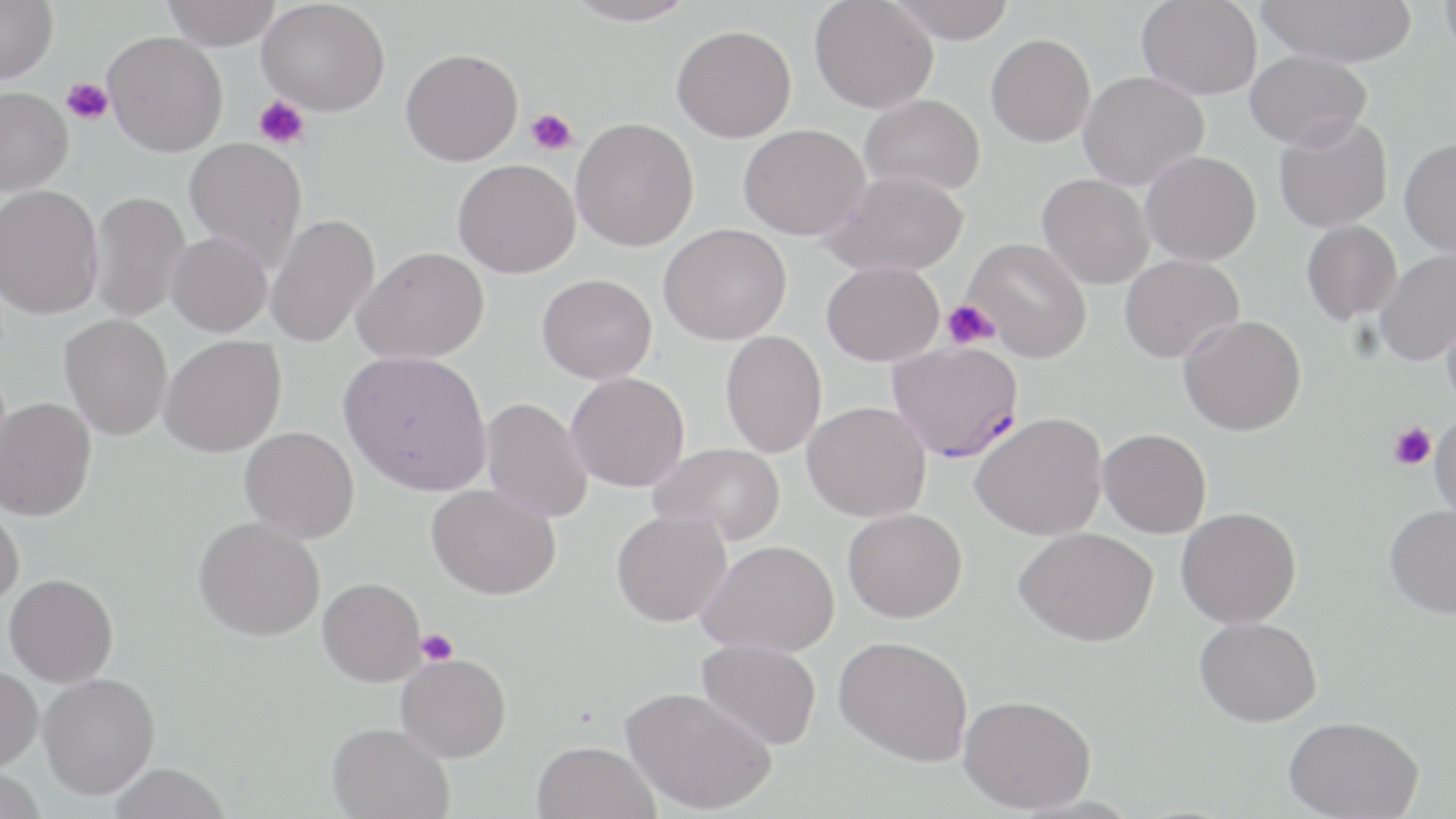

{
  "slide_level_diagnosis": "Plasmodium falciparum",
  "field_of_view": "single",
  "uninfected_red_blood_cell_locations": "approximate bounding boxes as (x1, y1, x2, y2) in pixels: (0, 0, 58, 83), (162, 0, 281, 50), (258, 0, 390, 116), (564, 0, 699, 27), (809, 0, 938, 114), (886, 0, 1016, 43), (1136, 0, 1263, 99), (1256, 0, 1417, 67), (1438, 1, 1456, 57), (672, 24, 796, 143), (103, 31, 228, 157), (986, 33, 1096, 147), (400, 48, 523, 166), (1245, 50, 1372, 150), (1078, 71, 1209, 190), (0, 87, 73, 195), (859, 94, 985, 196), (1273, 114, 1393, 233), (570, 117, 699, 251), (738, 123, 870, 240), (184, 137, 307, 269), (1399, 138, 1456, 257), (1140, 150, 1262, 266), (453, 159, 580, 278), (822, 170, 969, 277), (1037, 174, 1155, 289), (0, 184, 104, 320), (88, 191, 190, 323), (264, 213, 380, 348), (1301, 219, 1402, 325), (658, 223, 791, 345), (165, 232, 272, 337), (962, 237, 1092, 363), (353, 246, 489, 364), (1375, 249, 1456, 365), (1119, 254, 1245, 363), (821, 260, 944, 366), (537, 273, 657, 384), (1442, 305, 1456, 414), (59, 313, 172, 440), (1178, 315, 1306, 436), (720, 330, 827, 458), (159, 334, 287, 458), (338, 350, 492, 495), (565, 371, 690, 492), (1, 397, 96, 521), (480, 397, 593, 523), (802, 401, 931, 522), (971, 413, 1107, 541), (1429, 413, 1456, 522), (239, 426, 359, 543), (1098, 428, 1211, 538), (649, 442, 786, 546), (427, 483, 560, 600), (0, 497, 24, 608), (1384, 503, 1456, 619), (843, 507, 967, 623), (1176, 507, 1301, 628), (611, 509, 732, 627), (193, 516, 325, 642), (1014, 527, 1158, 646), (698, 539, 839, 657), (4, 573, 119, 687), (317, 577, 427, 687), (1195, 616, 1322, 727), (834, 635, 973, 766), (696, 637, 822, 750), (396, 652, 512, 763), (0, 665, 43, 773), (38, 673, 161, 800), (620, 686, 776, 815), (958, 694, 1096, 813), (1283, 715, 1423, 819), (327, 721, 454, 818), (531, 740, 660, 819), (108, 762, 231, 819), (0, 767, 47, 819)",
  "plasmodium_falciparum_infected_red_blood_cell_locations": "approximate bounding boxes as (x1, y1, x2, y2) in pixels: (888, 340, 1024, 463)",
  "preparation": "thin blood smear",
  "stain": "May-Grünwald-Giemsa",
  "platelet_locations": "approximate bounding boxes as (x1, y1, x2, y2) in pixels: (61, 78, 113, 125), (253, 95, 310, 150), (526, 108, 578, 156), (942, 300, 1000, 349), (1388, 422, 1437, 470), (416, 628, 458, 665)",
  "modality": "optical microscopy",
  "magnification": "1000x",
  "image_size": "1456×819 pixels"
}